Name the parasite shown.
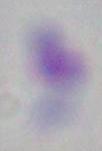

This is Toxoplasma gondii.

{
  "magnification": "1000x",
  "modality": "micrograph"
}